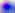
Summary:
  - Magnification: 400x
  - Modality: photomicrograph
  - Identification: Toxoplasma gondii